Describe the morphology of the red blood cells.
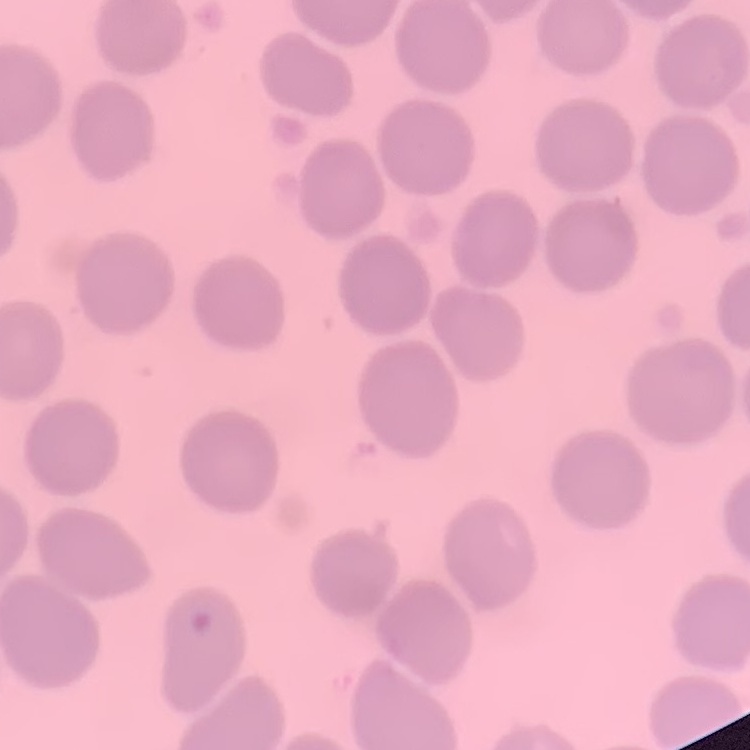
They show no rouleaux formation.

Thin blood smear. Field's or Giemsa stain. One tile cut from a larger photomicrograph.